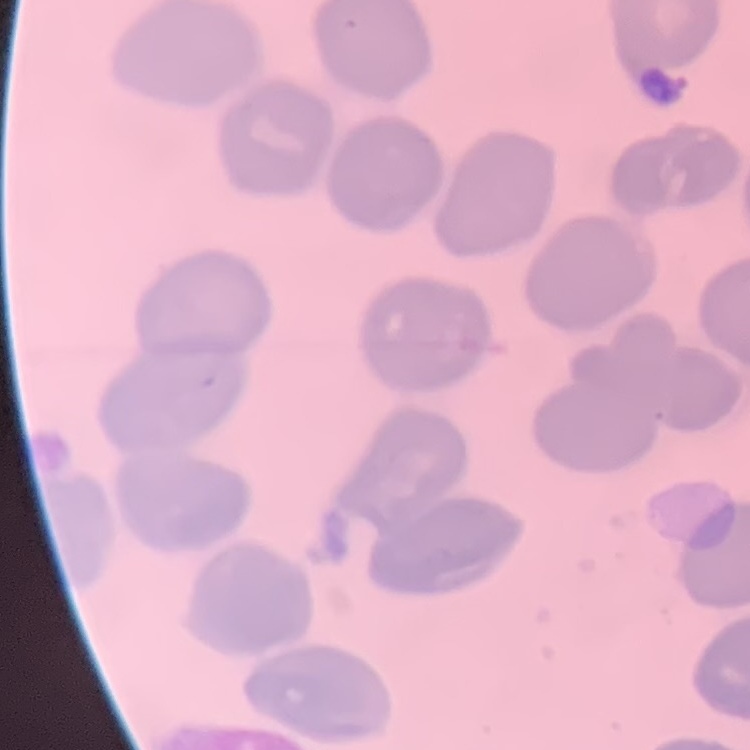

{
  "red_blood_cell_morphology": "no rouleaux formation",
  "preparation": "thin blood smear",
  "stain": "Field's or Giemsa",
  "image_type": "square crop of a larger photomicrograph"
}